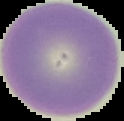

Malaria status: uninfected. From a thin blood film. Image is 124×121 pixels. Segmented cell region on a black background.